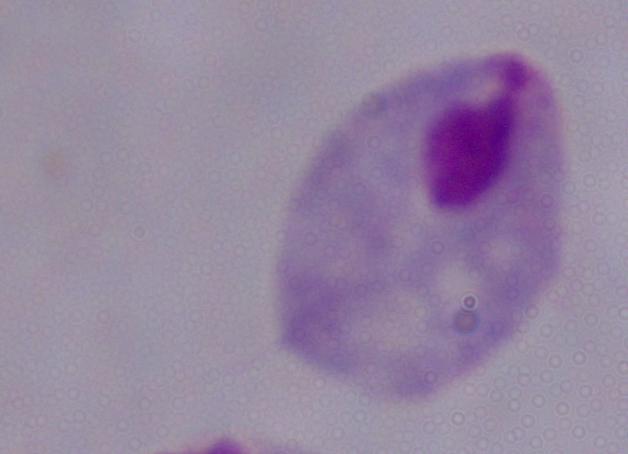
Summary:
  - Identification: trichomonad
  - Magnification: 1000x
  - Modality: photomicrograph